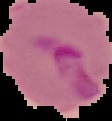
Image is 112×121 pixels. Segmented cell region on a black background. Malaria status: parasitized. From a thin blood smear.